Look for Plasmodium parasites.
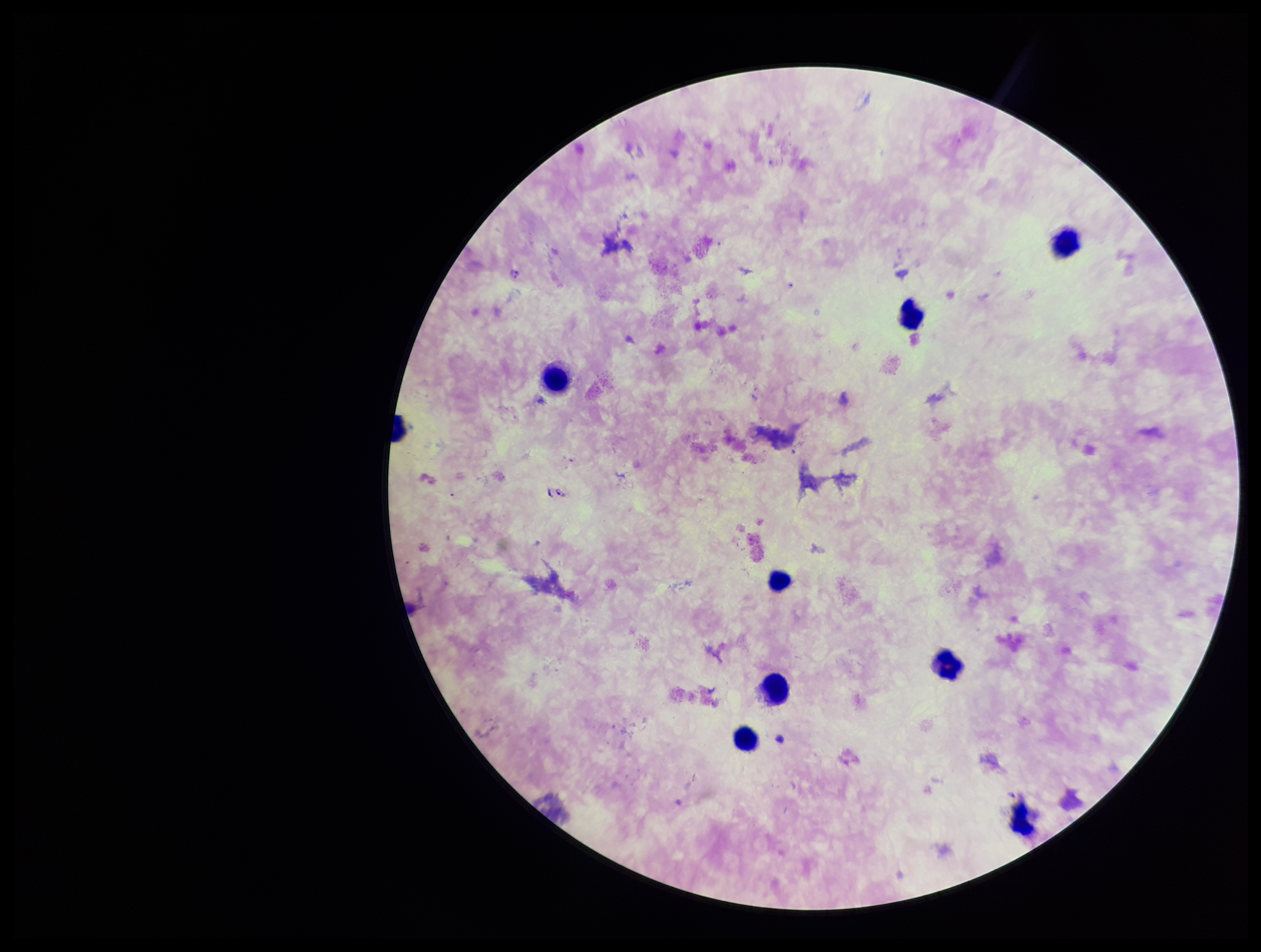
Identified.

Leukocyte count: 9. Image is 1261×952 pixels. Smartphone photograph taken through the eyepiece of a microscope. Preparation: thick smear. Parasite count: 3. Stained with Giemsa. Patient malaria status: positive. Single field of view. Species reported for this patient: Plasmodium falciparum.